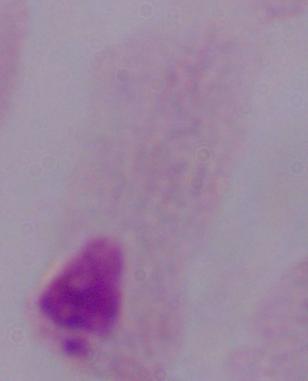
magnification = 1000x
modality = micrograph
identification = trichomonad